Describe the morphology of the red blood cells.
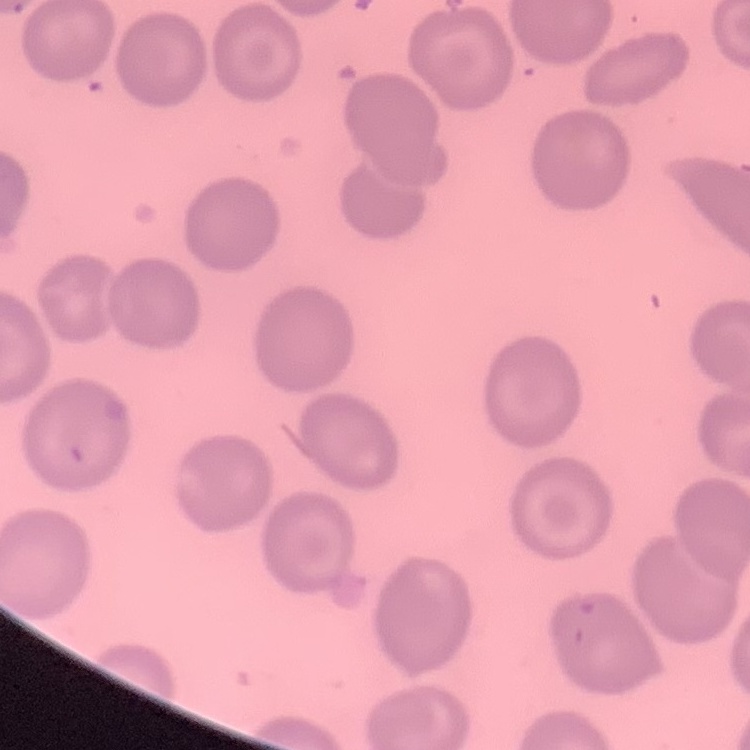
They show no rouleaux formation.

Summary:
  - Stain: Field's or Giemsa
  - Image type: one tile cut from a larger photomicrograph
  - Preparation: thin peripheral smear